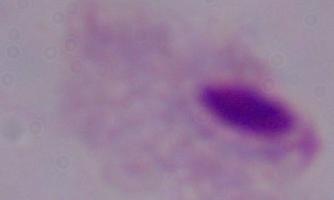

magnification = 1000x
identification = trichomonad
modality = micrograph